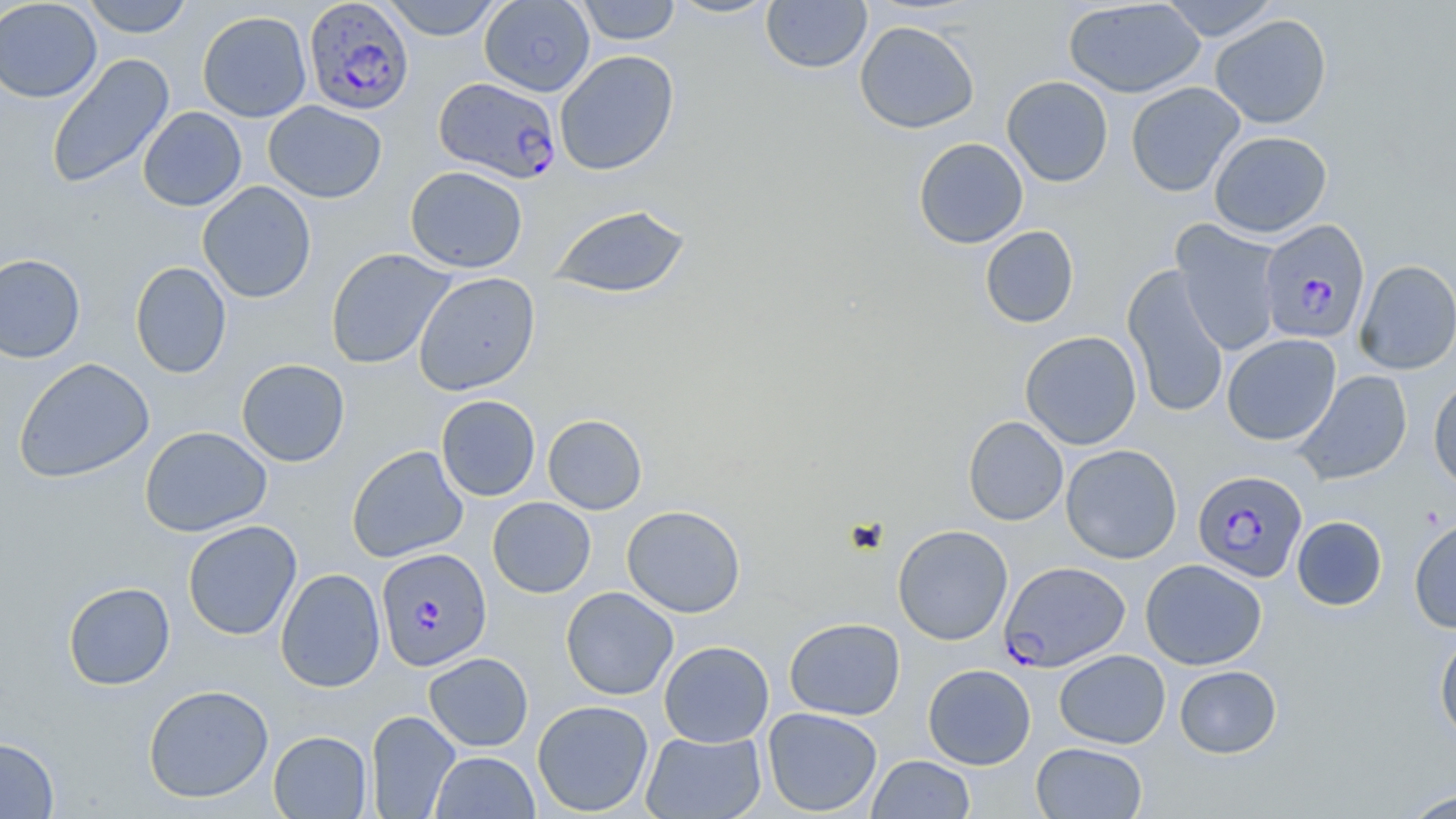

slide-level diagnosis = Plasmodium falciparum
stain = May-Grünwald-Giemsa
modality = optical microscopy
magnification = 1000x
uninfected red blood cell locations = approximate bounding boxes as (x1, y1, x2, y2) in pixels: (81, 0, 194, 37), (380, 0, 504, 40), (479, 0, 595, 97), (575, 0, 681, 45), (665, 0, 779, 19), (1158, 0, 1281, 41), (0, 1, 102, 103), (761, 1, 872, 73), (1062, 1, 1206, 98), (197, 11, 312, 122), (1210, 14, 1332, 129), (854, 20, 980, 134), (554, 49, 679, 176), (46, 53, 175, 190), (1001, 75, 1113, 187), (1126, 82, 1245, 197), (263, 101, 387, 203), (137, 106, 247, 211), (1209, 131, 1332, 238), (913, 137, 1028, 249), (405, 166, 528, 273), (197, 181, 317, 304), (547, 203, 692, 299), (1171, 221, 1284, 356), (980, 226, 1079, 328), (325, 248, 455, 370), (0, 253, 85, 363), (1354, 260, 1456, 374), (130, 261, 232, 379), (1122, 264, 1229, 419), (413, 272, 541, 396), (1019, 331, 1142, 450), (1222, 334, 1341, 446), (14, 357, 155, 484), (236, 359, 350, 467), (1293, 370, 1413, 486), (1428, 376, 1456, 493), (436, 395, 540, 501), (542, 414, 647, 515), (963, 415, 1068, 525), (139, 426, 272, 536), (1061, 444, 1182, 564), (346, 445, 468, 563), (487, 497, 596, 598), (622, 505, 746, 618), (1291, 516, 1387, 611), (1409, 516, 1456, 633), (182, 520, 302, 641), (892, 524, 1013, 645), (1141, 559, 1267, 670), (275, 568, 386, 693), (62, 581, 176, 690), (561, 586, 678, 700), (784, 617, 905, 720), (1434, 629, 1456, 746), (659, 640, 774, 747), (1054, 649, 1171, 749), (424, 652, 533, 752), (922, 664, 1036, 769), (1174, 665, 1282, 758), (143, 684, 273, 803), (532, 700, 654, 815), (762, 707, 883, 816), (366, 710, 461, 819), (268, 730, 372, 818), (640, 731, 766, 819), (0, 736, 59, 818), (1031, 742, 1146, 818), (430, 752, 540, 818), (867, 755, 975, 818), (1399, 788, 1456, 818)
field of view = single
preparation = thin blood film
image size = 1456×819 pixels
Plasmodium falciparum-infected red blood cell locations = approximate bounding boxes as (x1, y1, x2, y2) in pixels: (303, 1, 415, 115), (434, 77, 562, 183), (1258, 219, 1371, 344), (1193, 470, 1308, 582), (375, 547, 492, 672), (999, 560, 1130, 672)